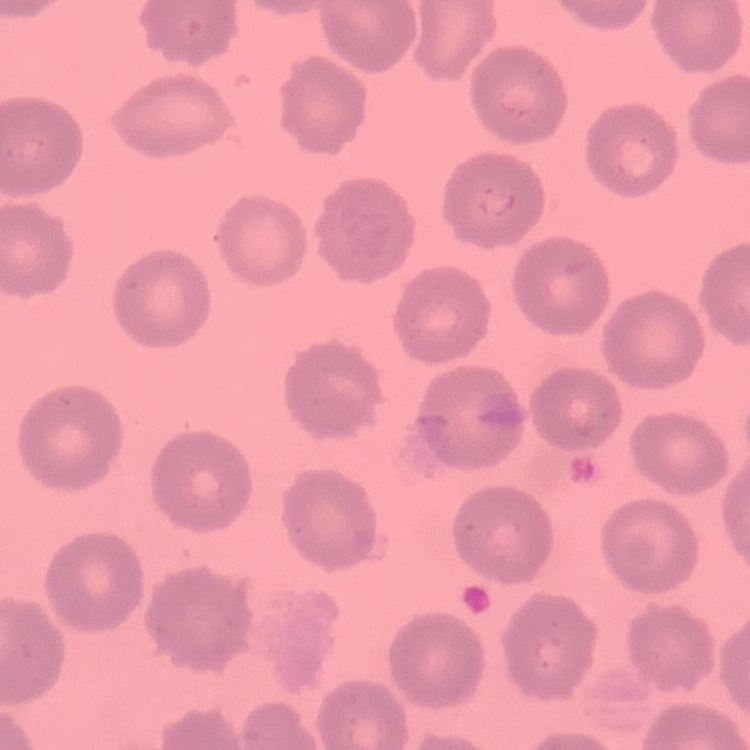
The red blood cells exhibit no rouleaux formation. Field's or Giemsa stain. Thin peripheral smear. Square crop of a larger photomicrograph.